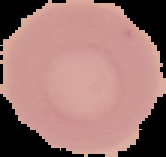

Segmented cell region on a black background. Image is 166×157 pixels. From a thin blood film. Malaria status: uninfected.